Identify the blood parasite species.
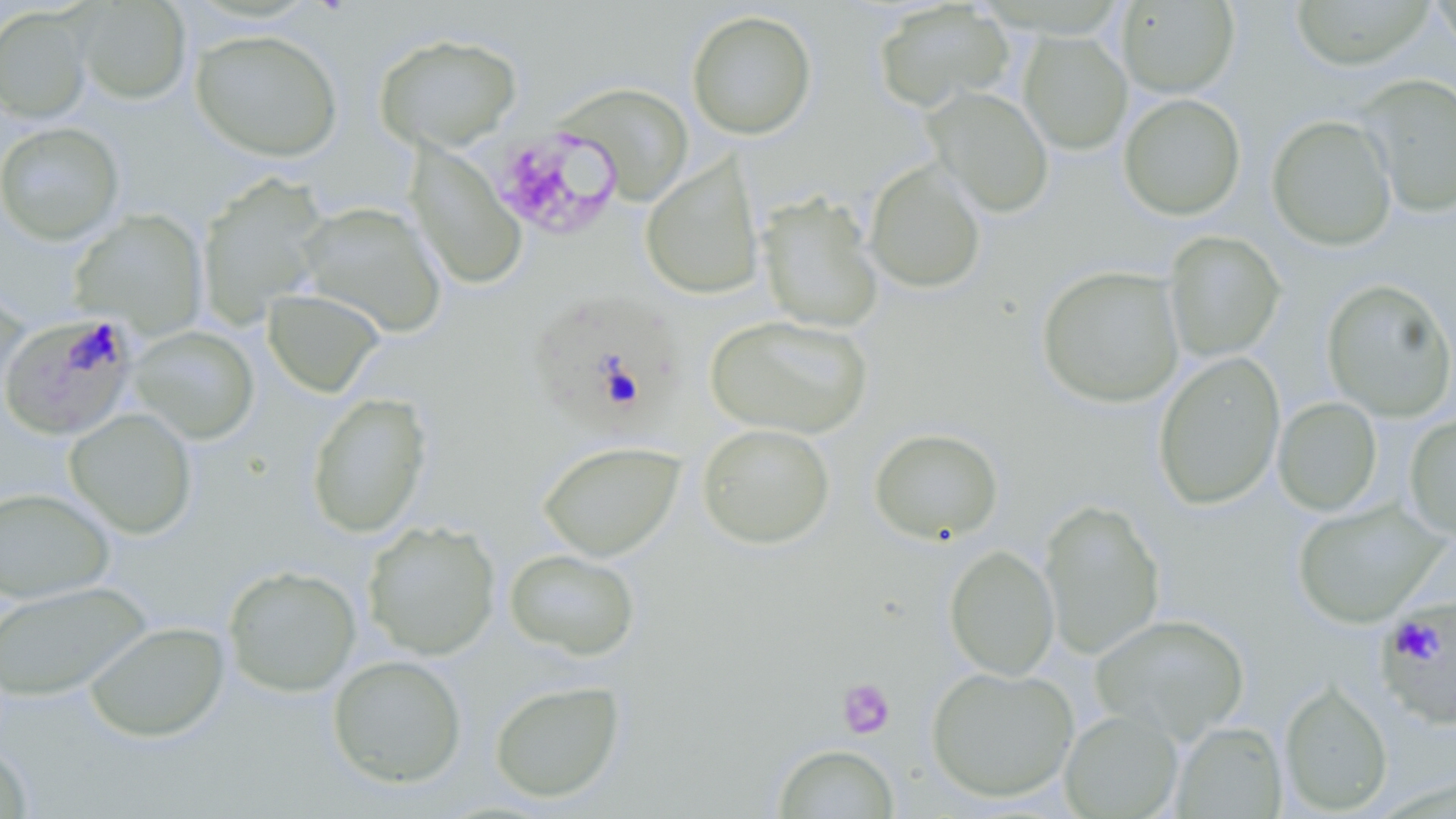
Plasmodium falciparum.

stain: May-Grünwald-Giemsa
plasmodium_falciparum_infected_red_blood_cell_locations: 'approximate bounding boxes as named x1/y1/x2/y2 corners in pixels: (x1=534, y1=291, x2=695, y2=443), (x1=8, y1=311, x2=149, y2=440), (x1=1375, y1=594, x2=1456, y2=729)'
image_size: 1456×819 pixels
platelet_locations: 'approximate bounding boxes as named x1/y1/x2/y2 corners in pixels: (x1=492, y1=128, x2=622, y2=240), (x1=836, y1=678, x2=896, y2=739)'
field_of_view: single
uninfected_red_blood_cell_locations: 'approximate bounding boxes as named x1/y1/x2/y2 corners in pixels: (x1=74, y1=0, x2=193, y2=105), (x1=1290, y1=0, x2=1433, y2=70), (x1=1430, y1=0, x2=1456, y2=57), (x1=872, y1=1, x2=1015, y2=113), (x1=1117, y1=1, x2=1239, y2=98), (x1=0, y1=7, x2=93, y2=125), (x1=686, y1=9, x2=818, y2=141), (x1=189, y1=28, x2=343, y2=162), (x1=1018, y1=30, x2=1133, y2=155), (x1=372, y1=32, x2=524, y2=154), (x1=1355, y1=72, x2=1456, y2=218), (x1=552, y1=82, x2=695, y2=205), (x1=924, y1=86, x2=1055, y2=218), (x1=1118, y1=93, x2=1246, y2=221), (x1=1266, y1=114, x2=1398, y2=251), (x1=0, y1=121, x2=126, y2=246), (x1=405, y1=142, x2=528, y2=291), (x1=639, y1=154, x2=765, y2=300), (x1=864, y1=159, x2=987, y2=294), (x1=195, y1=174, x2=331, y2=329), (x1=756, y1=191, x2=884, y2=334), (x1=296, y1=200, x2=448, y2=339), (x1=68, y1=209, x2=209, y2=338), (x1=1163, y1=231, x2=1286, y2=361), (x1=1036, y1=264, x2=1185, y2=408), (x1=0, y1=277, x2=29, y2=405), (x1=1321, y1=278, x2=1456, y2=422), (x1=262, y1=287, x2=386, y2=398), (x1=704, y1=314, x2=873, y2=439), (x1=128, y1=325, x2=260, y2=444), (x1=1152, y1=351, x2=1286, y2=511), (x1=305, y1=392, x2=433, y2=538), (x1=1272, y1=396, x2=1383, y2=516), (x1=64, y1=408, x2=198, y2=539), (x1=1404, y1=414, x2=1456, y2=541), (x1=697, y1=422, x2=836, y2=549), (x1=868, y1=427, x2=1004, y2=545), (x1=537, y1=439, x2=685, y2=562), (x1=0, y1=486, x2=116, y2=604), (x1=1039, y1=497, x2=1165, y2=660), (x1=1292, y1=499, x2=1448, y2=629), (x1=362, y1=520, x2=501, y2=661), (x1=944, y1=543, x2=1059, y2=681), (x1=504, y1=548, x2=641, y2=660), (x1=222, y1=564, x2=363, y2=698), (x1=0, y1=580, x2=153, y2=700), (x1=1090, y1=613, x2=1251, y2=742), (x1=84, y1=620, x2=231, y2=742), (x1=326, y1=654, x2=468, y2=789), (x1=926, y1=664, x2=1079, y2=803), (x1=488, y1=679, x2=625, y2=804), (x1=1279, y1=679, x2=1394, y2=816), (x1=1059, y1=708, x2=1184, y2=819), (x1=1172, y1=721, x2=1288, y2=818), (x1=0, y1=742, x2=35, y2=818), (x1=771, y1=743, x2=901, y2=818)'
magnification: 1000x
preparation: thin blood film
modality: light microscopy